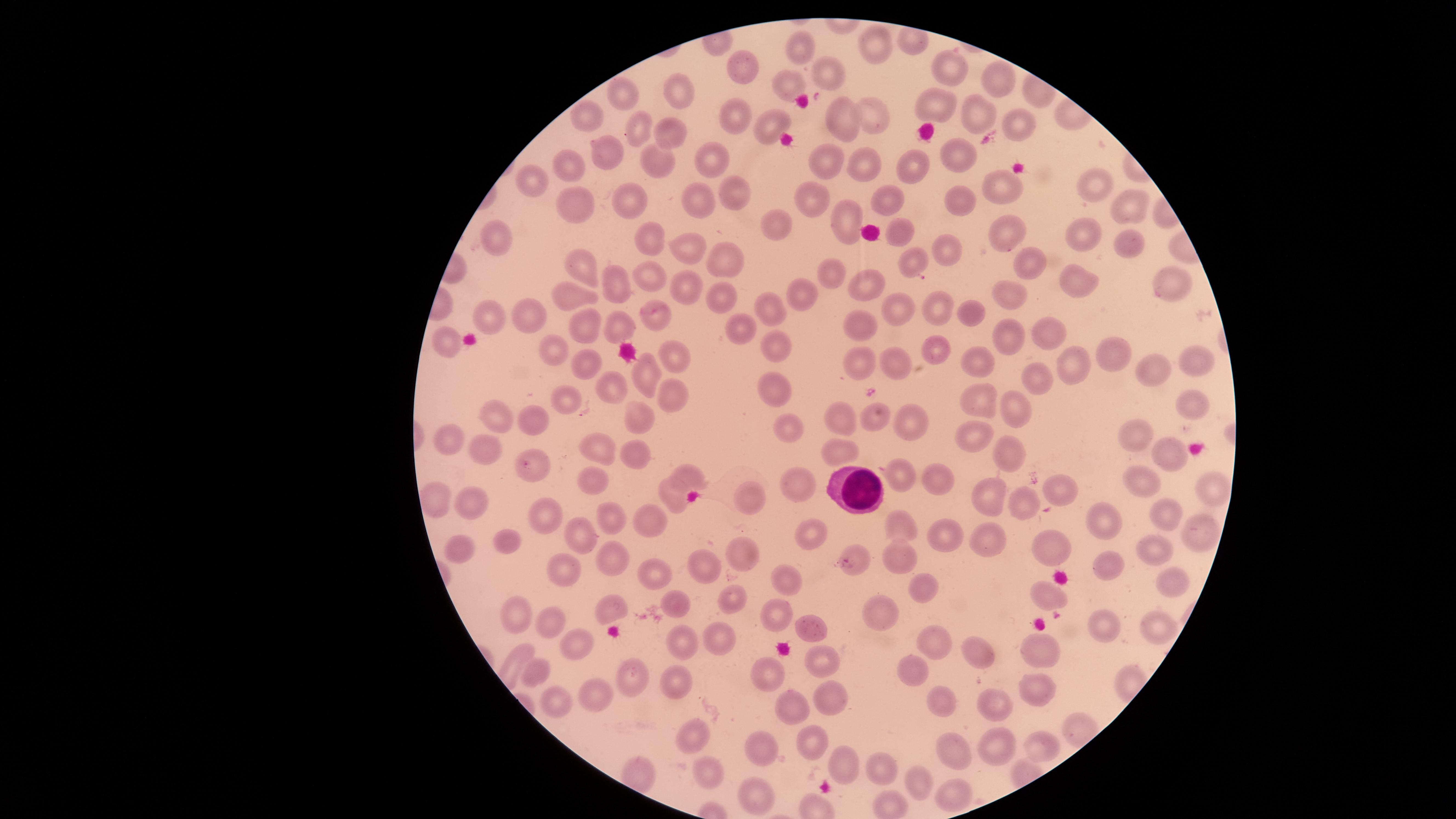

Approximate marker points, in pixels from the top-left corner. White blood cells: (x=857, y=489). Uninfected red blood cells: (x=878, y=43), (x=799, y=45), (x=747, y=62), (x=955, y=70), (x=832, y=74), (x=788, y=81), (x=1000, y=82), (x=675, y=92), (x=624, y=93), (x=938, y=106), (x=841, y=117), (x=584, y=118), (x=878, y=118), (x=982, y=118), (x=735, y=122), (x=770, y=124), (x=1020, y=124), (x=639, y=125), (x=670, y=137), (x=960, y=154), (x=610, y=155), (x=711, y=158), (x=558, y=164), (x=655, y=164), (x=822, y=164), (x=865, y=164), (x=907, y=172), (x=534, y=183), (x=1093, y=185), (x=730, y=187), (x=1006, y=187), (x=625, y=199), (x=809, y=200), (x=567, y=202), (x=699, y=202), (x=884, y=205), (x=968, y=206), (x=1125, y=210), (x=848, y=214), (x=778, y=217), (x=1010, y=229), (x=897, y=235), (x=1091, y=235), (x=686, y=241), (x=501, y=243), (x=1133, y=243), (x=649, y=247), (x=953, y=251), (x=722, y=254), (x=579, y=264), (x=918, y=265), (x=1023, y=267), (x=828, y=273), (x=655, y=281), (x=1077, y=282), (x=612, y=284), (x=1165, y=285), (x=864, y=289), (x=684, y=290), (x=572, y=293), (x=799, y=294), (x=713, y=298), (x=1003, y=299), (x=936, y=306), (x=773, y=312), (x=900, y=312), (x=976, y=314), (x=528, y=315), (x=654, y=317), (x=484, y=318), (x=580, y=324), (x=860, y=326), (x=628, y=329), (x=1052, y=333), (x=734, y=334), (x=1008, y=339), (x=450, y=345), (x=553, y=345), (x=775, y=348), (x=1112, y=348), (x=930, y=350), (x=1183, y=354), (x=675, y=355), (x=862, y=358), (x=891, y=364), (x=981, y=365), (x=584, y=366), (x=1071, y=367), (x=1147, y=371), (x=651, y=375), (x=1033, y=376), (x=613, y=387), (x=772, y=393), (x=677, y=401), (x=573, y=403), (x=975, y=405), (x=1015, y=405), (x=1193, y=406), (x=873, y=412), (x=498, y=415), (x=838, y=416), (x=533, y=419), (x=642, y=420), (x=907, y=421), (x=784, y=426), (x=968, y=430), (x=449, y=438), (x=1144, y=438), (x=605, y=444), (x=835, y=447), (x=485, y=448), (x=1006, y=449), (x=1166, y=456), (x=639, y=457), (x=691, y=473), (x=585, y=478), (x=903, y=479), (x=940, y=481), (x=1140, y=483), (x=795, y=485), (x=1057, y=491), (x=991, y=493), (x=430, y=494), (x=753, y=495), (x=1213, y=496), (x=670, y=500), (x=1020, y=504), (x=469, y=505), (x=611, y=514), (x=1159, y=515), (x=650, y=517), (x=548, y=520), (x=1098, y=521), (x=901, y=526), (x=1195, y=531), (x=582, y=535), (x=941, y=536), (x=808, y=538), (x=986, y=538), (x=507, y=543), (x=1052, y=546), (x=462, y=548), (x=1154, y=552), (x=896, y=557), (x=749, y=559), (x=858, y=564), (x=1105, y=565), (x=558, y=569), (x=709, y=570), (x=657, y=574), (x=1162, y=581), (x=921, y=582), (x=787, y=588), (x=1047, y=598), (x=675, y=599), (x=729, y=603), (x=880, y=605), (x=512, y=611), (x=611, y=611), (x=777, y=615), (x=552, y=621), (x=1158, y=624), (x=810, y=625), (x=1100, y=628), (x=715, y=638), (x=935, y=639), (x=578, y=641), (x=682, y=646), (x=977, y=649), (x=1045, y=651), (x=819, y=663), (x=536, y=666), (x=913, y=675), (x=776, y=677), (x=628, y=678), (x=675, y=678), (x=1031, y=693), (x=590, y=695), (x=833, y=696), (x=561, y=704), (x=939, y=704), (x=793, y=707), (x=994, y=707), (x=694, y=734), (x=809, y=743), (x=1043, y=743), (x=1000, y=747), (x=761, y=753), (x=960, y=754), (x=879, y=764), (x=840, y=768), (x=717, y=771), (x=916, y=782), (x=948, y=792), (x=753, y=798). One field of view of the specimen. Presence: no malaria parasites identified. Thin blood smear. Circular visible region. Giemsa-stained preparation. Image is 1456×819 pixels. Smartphone photograph through the microscope eyepiece.